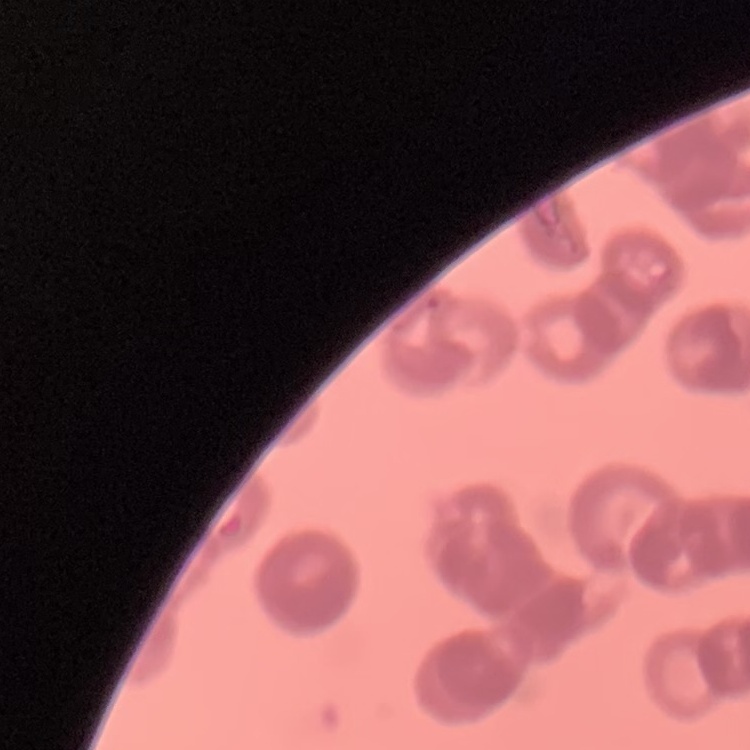

Summary:
  - Red blood cell morphology: rouleaux formation
  - Stain: Field's or Giemsa
  - Preparation: thin peripheral smear
  - Image type: one tile cut from a larger photomicrograph